Report the malaria status of this cell.
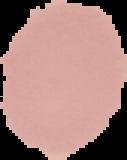
Uninfected.

Cell region segmented out of the field of view; the surrounding area is masked to black. Image is 127×160 pixels. From a thin blood film.